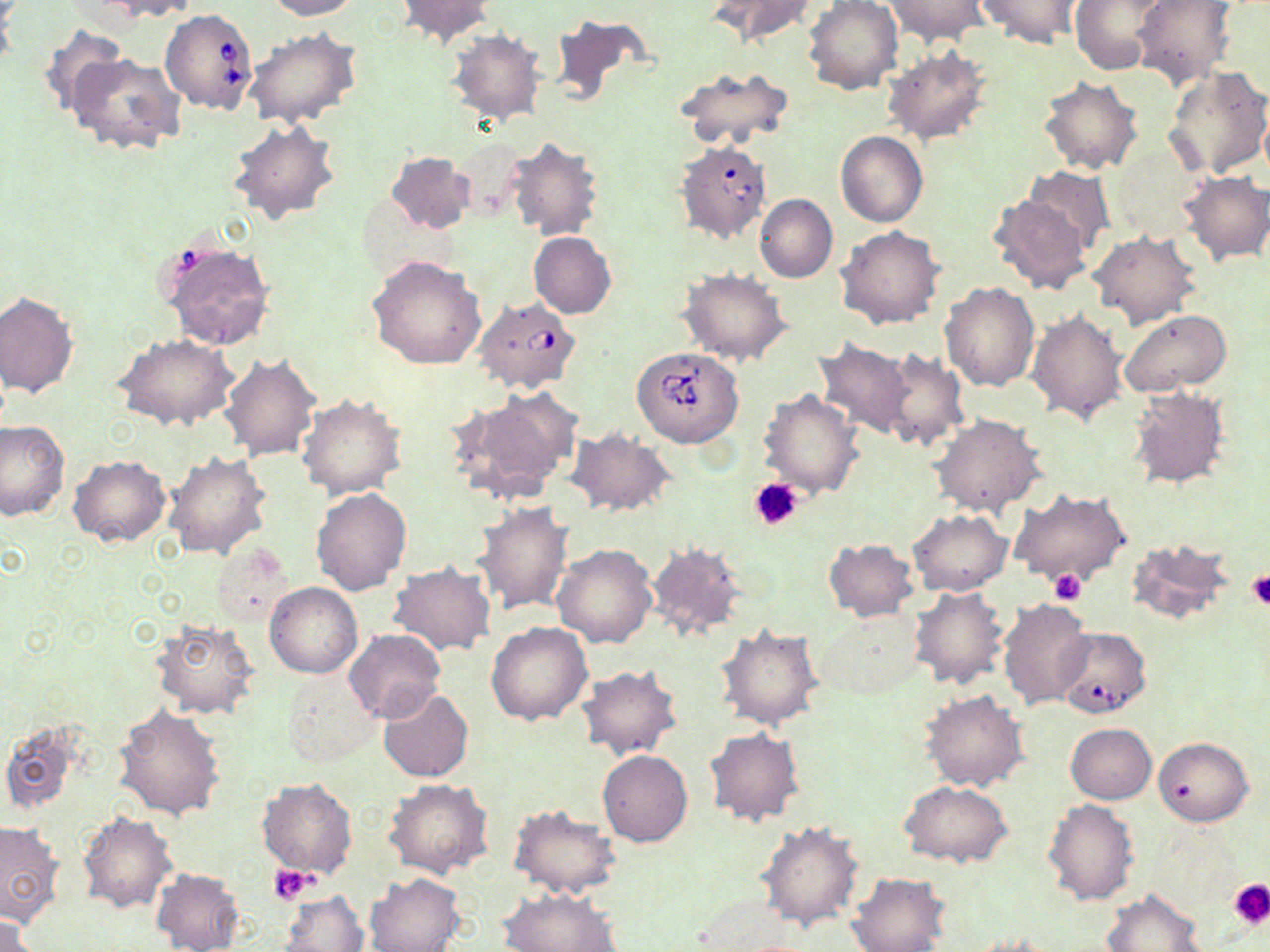

Summary:
  - Coordinate format: approximate bounding boxes as (x1, y1, x2, y2) in pixels
  - Babesia divergens-infected red blood cell locations: (160, 9, 258, 114), (673, 140, 772, 244), (473, 297, 581, 394), (632, 345, 743, 448), (1052, 626, 1146, 718)
  - Uninfected red blood cell locations: (99, 0, 201, 20), (264, 0, 359, 20), (397, 0, 493, 46), (711, 0, 818, 46), (803, 0, 903, 95), (883, 0, 990, 46), (974, 0, 1088, 48), (1071, 0, 1171, 74), (1130, 1, 1236, 90), (547, 15, 654, 111), (36, 22, 128, 119), (244, 28, 362, 129), (448, 29, 545, 126), (882, 47, 993, 145), (69, 53, 185, 158), (675, 66, 795, 149), (1162, 66, 1270, 181), (1038, 76, 1143, 174), (228, 118, 341, 224), (836, 132, 928, 227), (451, 136, 528, 225), (507, 138, 604, 241), (1107, 142, 1207, 239), (385, 151, 473, 233), (1025, 167, 1113, 255), (1177, 171, 1270, 267), (988, 193, 1094, 294), (755, 194, 837, 282), (837, 227, 945, 330), (1088, 231, 1200, 330), (529, 232, 616, 318), (158, 240, 275, 350), (368, 255, 486, 369), (678, 268, 792, 365), (939, 283, 1039, 392), (0, 292, 79, 398), (1119, 308, 1232, 396), (1026, 309, 1128, 426), (114, 333, 239, 431), (813, 339, 918, 441), (879, 349, 968, 452), (219, 352, 321, 459), (1125, 384, 1232, 491), (452, 386, 582, 503), (758, 389, 865, 500), (296, 393, 407, 499), (932, 414, 1047, 517), (0, 421, 68, 521), (566, 427, 677, 518), (162, 450, 272, 560), (69, 455, 170, 548), (310, 488, 411, 595), (1009, 489, 1132, 589), (472, 502, 574, 617), (907, 509, 1012, 595), (822, 538, 918, 621), (1125, 538, 1234, 627), (644, 542, 748, 644), (212, 544, 294, 625), (551, 544, 657, 648), (387, 563, 496, 656), (265, 582, 362, 678), (908, 586, 1011, 691), (997, 597, 1093, 709), (813, 609, 925, 700), (149, 617, 259, 718), (485, 622, 593, 725), (716, 624, 824, 730), (344, 628, 445, 724), (576, 665, 682, 759), (282, 670, 378, 766), (377, 687, 473, 782), (921, 689, 1031, 793), (113, 705, 226, 821), (0, 720, 86, 815), (1065, 724, 1156, 803), (705, 726, 805, 825), (1153, 736, 1253, 826), (597, 750, 693, 847), (256, 778, 358, 879), (383, 779, 494, 879), (901, 781, 1013, 866), (1041, 799, 1139, 906), (508, 805, 621, 898), (78, 812, 177, 913), (0, 820, 65, 927), (755, 820, 863, 931), (151, 868, 244, 952), (847, 871, 951, 952), (363, 873, 466, 951), (498, 888, 623, 951), (1101, 889, 1207, 952), (277, 891, 371, 951), (0, 912, 42, 951)
  - Platelet locations: (749, 476, 803, 531), (1049, 568, 1085, 605), (1245, 570, 1270, 609), (269, 865, 315, 905), (1228, 878, 1270, 927)
  - Slide-level diagnosis: Babesia divergens
  - Image size: 1270×952 pixels
  - Field of view: single
  - Modality: light microscopy
  - Preparation: thin blood film
  - Stain: May-Grünwald-Giemsa
  - Magnification: 1000x